Comment on the morphology of the red blood cells.
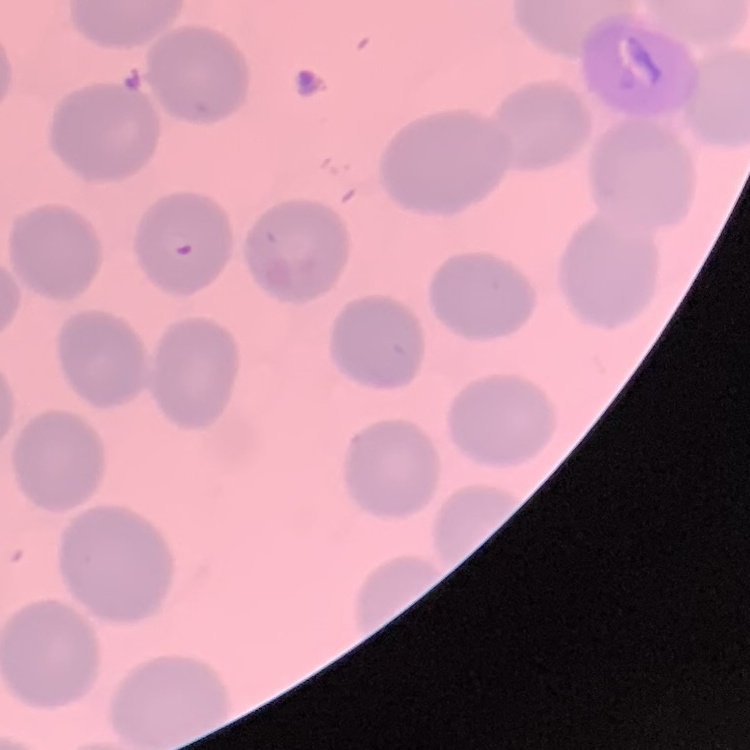

They show no rouleaux formation.

Stained with either Field's or Giemsa. Thin peripheral smear. One tile cut from a larger photomicrograph.